Outline every leukocyte.
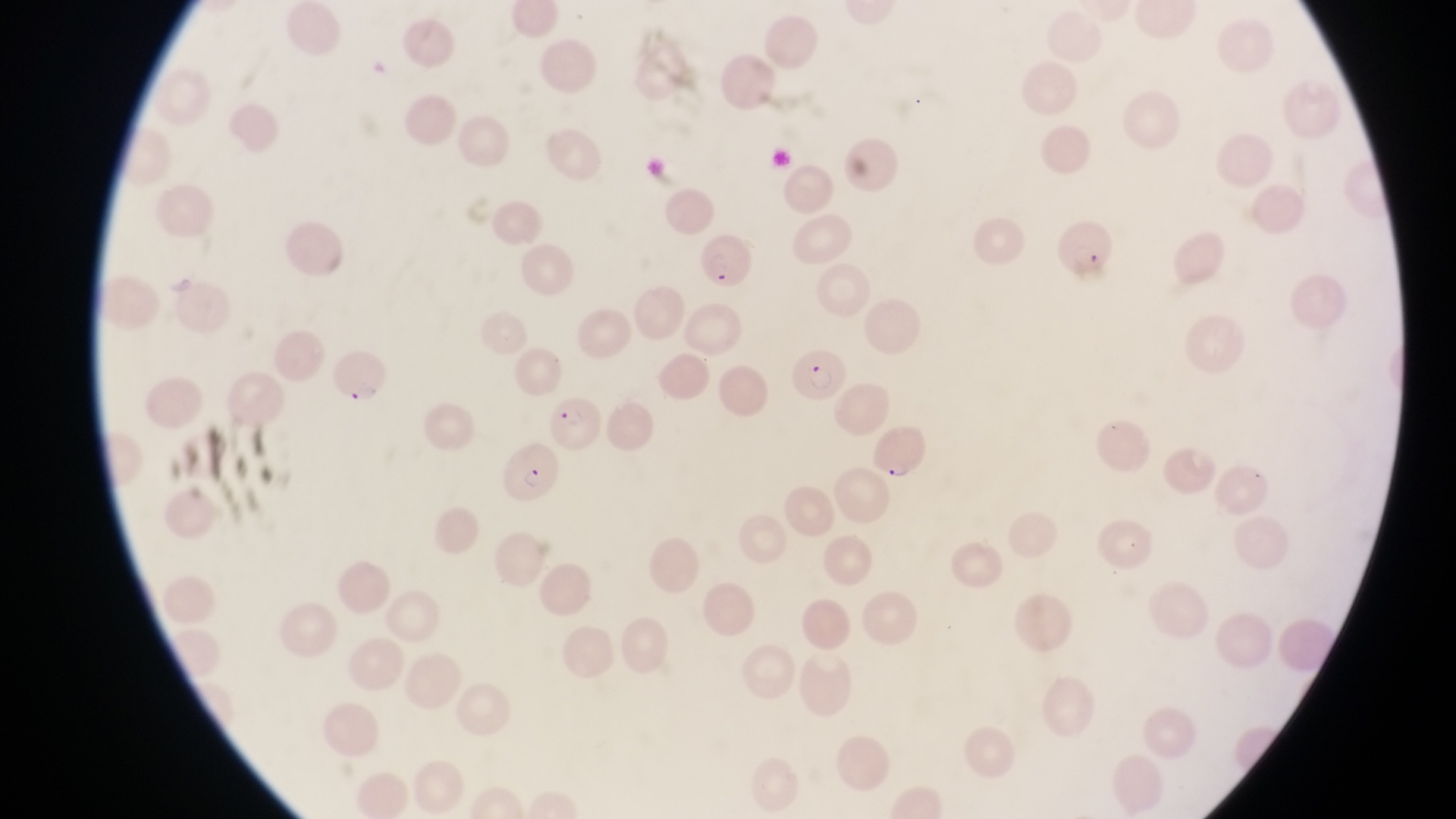
No leukocytes observed.

Approximate bounding boxes as left top right bottom in pixels.
Summary:
  - Parasitised red blood cell locations: 1059 217 1115 284; 698 232 754 295; 788 343 844 406; 325 349 391 407; 545 391 604 454; 871 419 931 477; 502 439 555 503
  - Image size: 1456×819 pixels
  - Capture: smartphone photograph through the eyepiece of an Olympus CX-23 microscope
  - Country: Uganda
  - Magnification: 1000x
  - Field of view: single
  - Preparation: thin blood smear